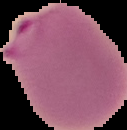
Summary:
  - Preparation: thin blood film
  - Image size: 127×130 pixels
  - Malaria status: parasitized
  - Image type: segmented cell region on a black background